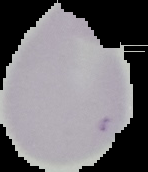

malaria status = uninfected
image size = 148×172 pixels
preparation = thin blood film
image type = segmented cell region with the area outside set to black